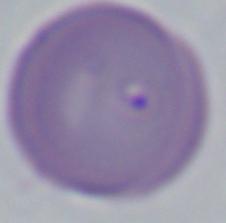

modality = photomicrograph
identification = Babesia
magnification = 1000x